Name the blood parasite species.
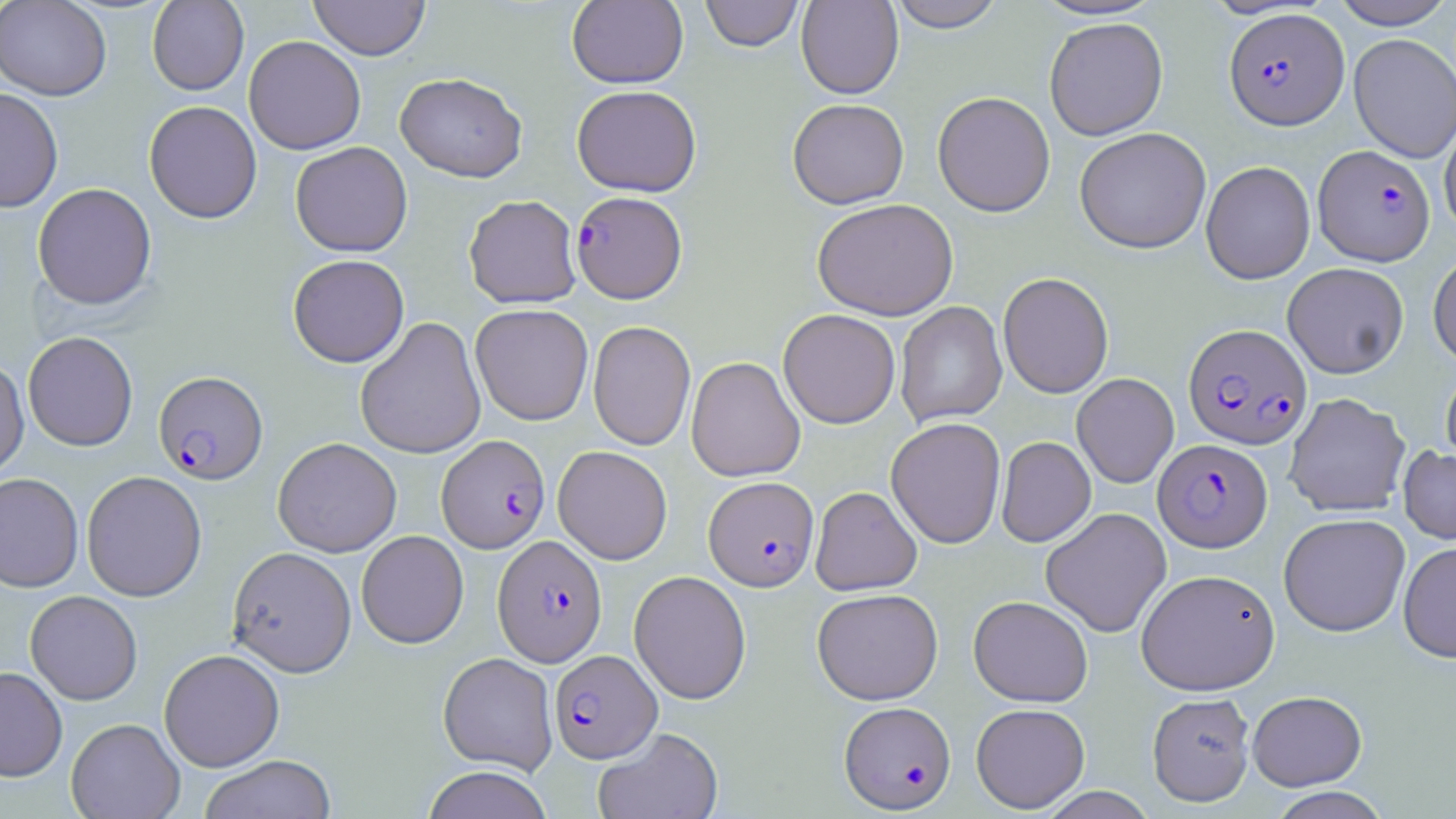
Plasmodium falciparum.

Summary:
  - Coordinate format: approximate bounding boxes as (x1, y1, x2, y2) in pixels
  - Uninfected red blood cell locations: (0, 0, 111, 100), (308, 0, 430, 60), (567, 0, 688, 88), (700, 0, 803, 51), (796, 0, 904, 99), (888, 0, 1006, 32), (1030, 0, 1167, 21), (1330, 0, 1454, 29), (147, 1, 249, 95), (1044, 17, 1168, 140), (1349, 33, 1456, 162), (243, 35, 366, 155), (395, 72, 527, 182), (572, 85, 702, 197), (0, 87, 64, 213), (932, 91, 1055, 217), (787, 98, 909, 209), (144, 100, 262, 224), (1439, 115, 1456, 238), (1074, 127, 1211, 253), (290, 141, 413, 257), (1200, 160, 1315, 284), (32, 183, 157, 310), (464, 194, 581, 308), (812, 198, 958, 321), (1428, 251, 1456, 366), (288, 254, 409, 367), (1282, 262, 1409, 378), (997, 272, 1114, 399), (895, 301, 1007, 427), (470, 304, 594, 425), (778, 309, 900, 429), (355, 316, 487, 460), (588, 320, 696, 451), (23, 331, 138, 451), (0, 356, 29, 478), (686, 356, 805, 482), (1441, 367, 1456, 473), (1072, 373, 1179, 488), (1284, 393, 1410, 517), (885, 417, 1006, 549), (996, 436, 1095, 547), (272, 437, 401, 557), (1398, 445, 1456, 544), (553, 446, 672, 564), (81, 470, 207, 601), (0, 472, 84, 593), (810, 486, 921, 596), (1040, 507, 1172, 637), (1279, 513, 1410, 636), (356, 531, 468, 648), (1398, 541, 1456, 663), (227, 546, 356, 677), (1135, 568, 1280, 695), (629, 570, 751, 704), (812, 588, 943, 705), (25, 590, 142, 705), (968, 595, 1093, 707), (159, 648, 285, 772), (438, 652, 558, 774), (0, 666, 68, 781), (1247, 690, 1366, 791), (1147, 692, 1255, 806), (971, 703, 1090, 813), (66, 718, 185, 818), (593, 727, 723, 819), (199, 755, 337, 818), (421, 766, 554, 819), (1034, 786, 1159, 818), (1269, 787, 1391, 819)
  - Plasmodium falciparum-infected red blood cell locations: (1224, 8, 1348, 130), (1314, 144, 1435, 266), (571, 190, 687, 303), (1183, 323, 1312, 449), (153, 370, 268, 485), (437, 435, 550, 553), (1153, 439, 1272, 553), (703, 476, 818, 591), (493, 535, 607, 667), (549, 649, 661, 763), (839, 700, 956, 813)
  - Preparation: thin blood smear
  - Stain: May-Grünwald-Giemsa
  - Image size: 1456×819 pixels
  - Modality: optical microscopy
  - Magnification: 1000x
  - Field of view: one of a larger specimen